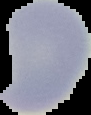
Summary:
  - Malaria status: uninfected
  - Preparation: thin blood smear
  - Image size: 91×115 pixels
  - Image type: segmented cell region on a black background